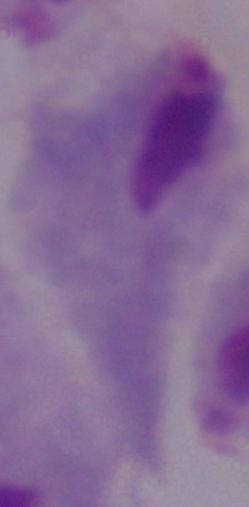
Captured at 1000x magnification. A trichomonad is shown. Photomicrograph.